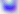

Summary:
  - Modality: photomicrograph
  - Magnification: 400x
  - Identification: Toxoplasma gondii